Report the malaria status of this cell.
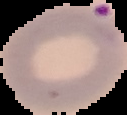
Parasitized.

Summary:
  - Preparation: thin blood smear
  - Image type: cell region segmented out of the field of view; surrounding area masked to black
  - Image size: 127×115 pixels